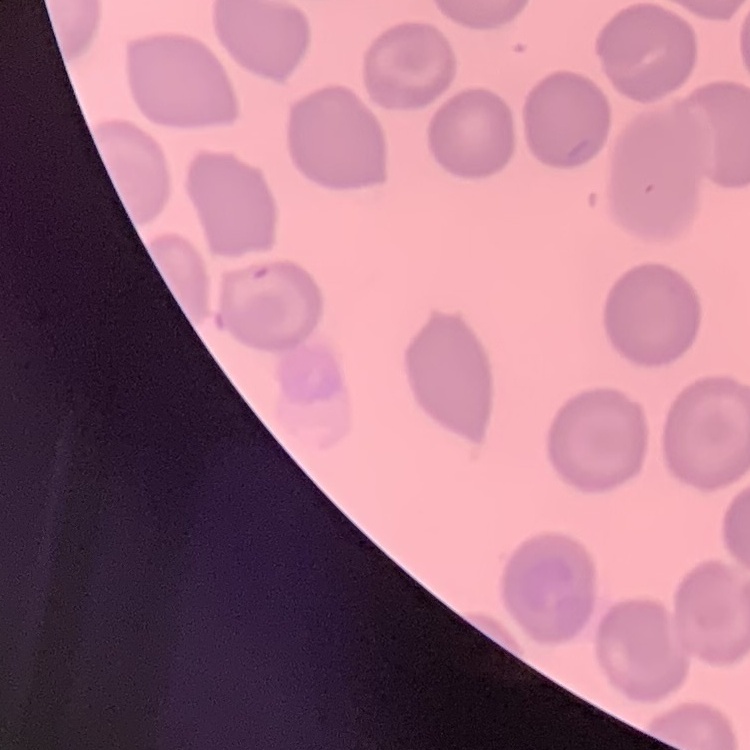

Summary:
  - Erythrocyte morphology: no rouleaux formation
  - Stain: Field's or Giemsa
  - Preparation: thin peripheral smear
  - Image type: one tile cut from a larger photomicrograph